State which parasite is depicted.
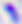
Toxoplasma gondii.

Micrograph. 400x magnification.